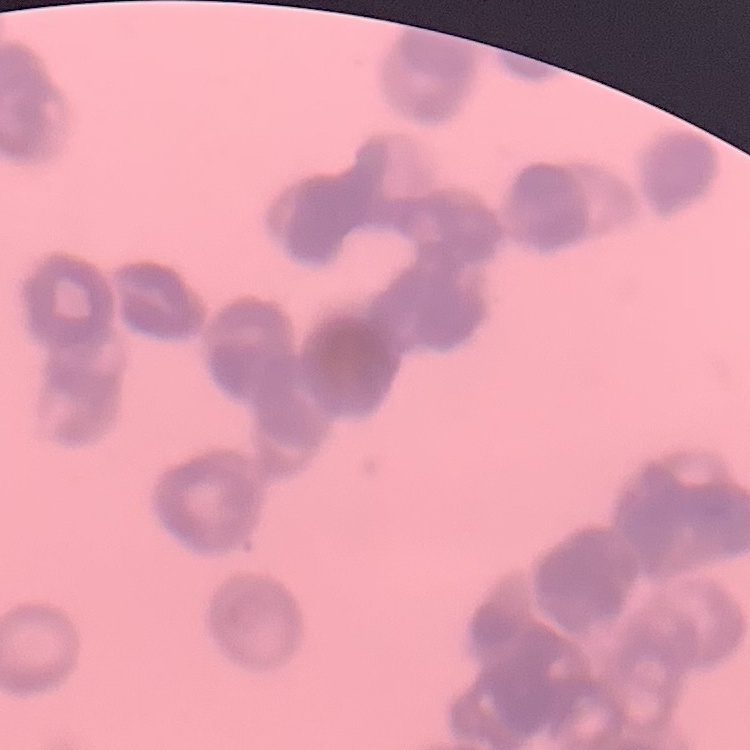

The red blood cells show rouleaux formation. Thin blood smear. Stained with either Field's or Giemsa. One tile cut from a larger photomicrograph.